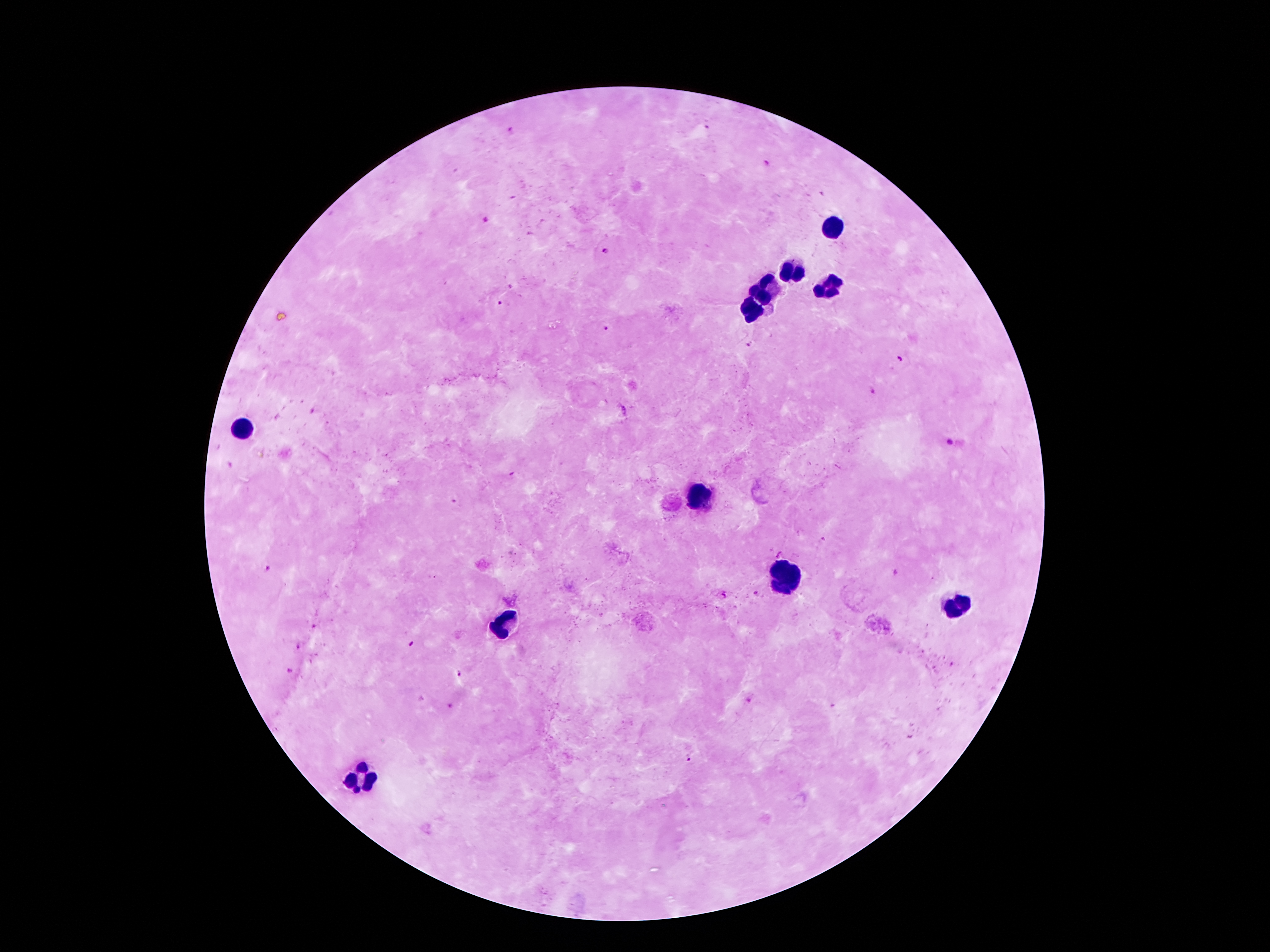
Approximate centers as (x, y) in pixels. Leukocyte locations: (829, 227), (798, 271), (771, 287), (827, 287), (753, 311), (244, 428), (700, 494), (777, 578), (958, 606), (500, 625), (359, 779). Malaria parasite locations: (708, 126), (512, 129), (765, 163), (486, 221), (606, 250), (501, 302), (606, 328), (750, 343), (900, 360), (873, 393), (948, 442), (511, 474), (269, 570), (896, 572), (755, 592), (725, 594), (313, 627), (414, 643), (297, 647), (291, 671), (458, 674), (748, 701), (451, 706), (689, 757). Image is 1270×952 pixels. Giemsa stain. Smartphone photograph taken through the microscope eyepiece. Single field of view. Patient malaria status: positive for Plasmodium falciparum. Thick blood film. 100x magnification.